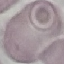
Summary:
  - Malaria status: uninfected
  - Capture: smartphone camera at the microscope eyepiece
  - Stain: Giemsa
  - Image type: cell patch, automatically extracted from a larger field of view and resized to 64 × 64 pixels
  - Preparation: thin smear